Locate and identify every blood parasite.
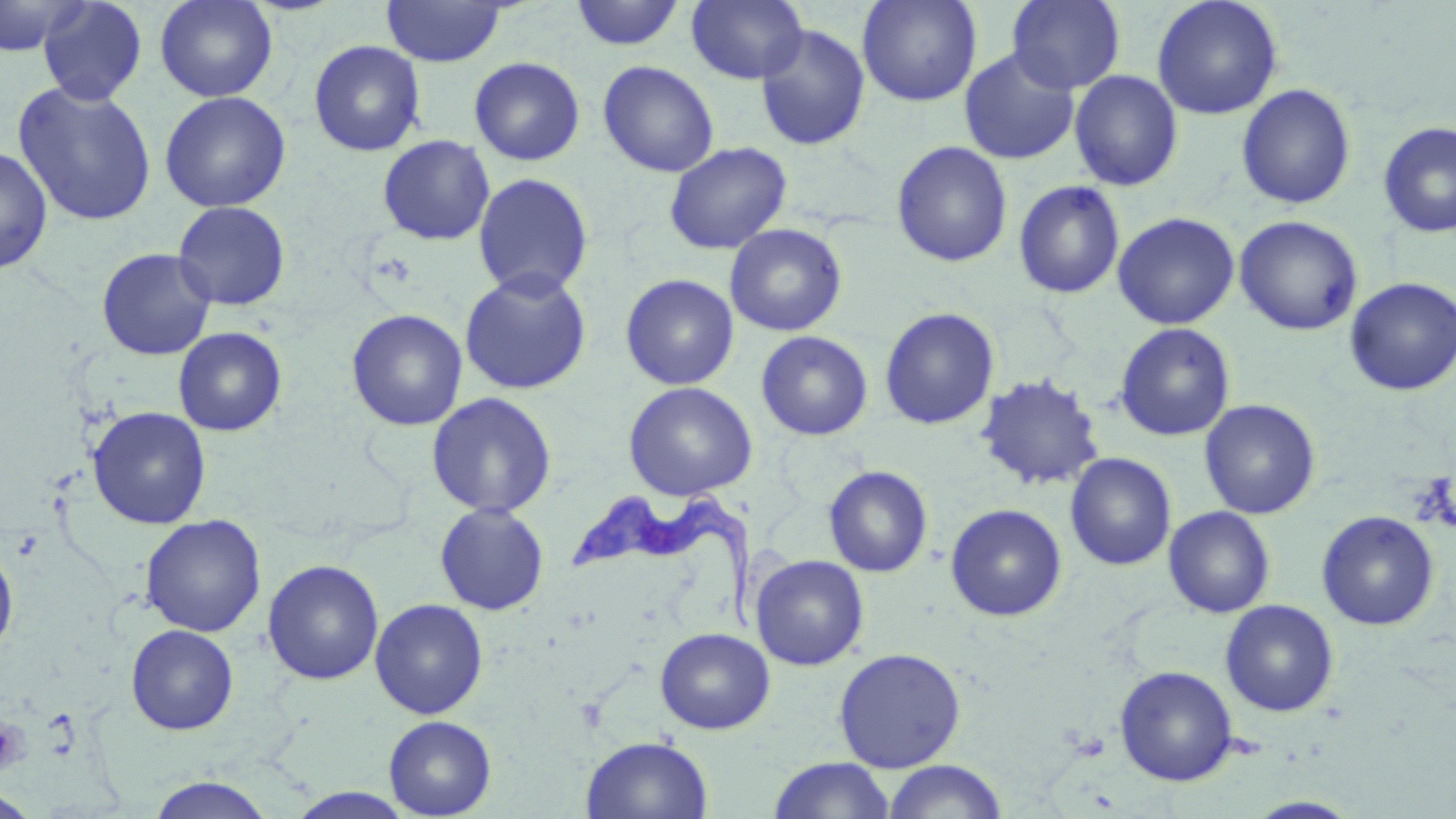
Approximate bounding boxes as named x1/y1/x2/y2 corners in pixels.
Trypanosoma brucei: (x1=568, y1=490, x2=762, y2=636).
No Plasmodium falciparum, Plasmodium ovale, Plasmodium malariae, Plasmodium vivax, or Babesia divergens observed.

slide_level_diagnosis: Trypanosoma brucei
stain: May-Grünwald-Giemsa
uninfected_red_blood_cell_locations: 'approximate bounding boxes as named x1/y1/x2/y2 corners in pixels: (x1=0, y1=0, x2=87, y2=57), (x1=37, y1=0, x2=148, y2=106), (x1=155, y1=0, x2=277, y2=102), (x1=381, y1=0, x2=508, y2=67), (x1=687, y1=0, x2=808, y2=84), (x1=856, y1=0, x2=983, y2=107), (x1=1006, y1=0, x2=1126, y2=94), (x1=1151, y1=0, x2=1284, y2=120), (x1=569, y1=1, x2=686, y2=51), (x1=755, y1=23, x2=871, y2=151), (x1=308, y1=40, x2=426, y2=157), (x1=959, y1=47, x2=1080, y2=165), (x1=468, y1=56, x2=585, y2=166), (x1=598, y1=60, x2=719, y2=177), (x1=1069, y1=70, x2=1183, y2=191), (x1=12, y1=81, x2=157, y2=226), (x1=1236, y1=84, x2=1356, y2=210), (x1=159, y1=91, x2=291, y2=213), (x1=1377, y1=122, x2=1456, y2=238), (x1=377, y1=134, x2=495, y2=246), (x1=664, y1=141, x2=792, y2=254), (x1=891, y1=141, x2=1013, y2=268), (x1=0, y1=146, x2=53, y2=274), (x1=472, y1=172, x2=594, y2=299), (x1=1013, y1=180, x2=1125, y2=299), (x1=172, y1=201, x2=291, y2=311), (x1=1113, y1=212, x2=1240, y2=330), (x1=1234, y1=215, x2=1363, y2=336), (x1=724, y1=223, x2=848, y2=336), (x1=96, y1=247, x2=217, y2=360), (x1=459, y1=268, x2=593, y2=395), (x1=620, y1=273, x2=739, y2=390), (x1=1344, y1=277, x2=1456, y2=396), (x1=879, y1=307, x2=1000, y2=430), (x1=346, y1=309, x2=468, y2=431), (x1=1114, y1=322, x2=1235, y2=442), (x1=173, y1=327, x2=287, y2=436), (x1=755, y1=331, x2=874, y2=441), (x1=976, y1=373, x2=1104, y2=491), (x1=622, y1=381, x2=758, y2=501), (x1=426, y1=392, x2=558, y2=518), (x1=1199, y1=398, x2=1321, y2=519), (x1=87, y1=407, x2=212, y2=530), (x1=1065, y1=452, x2=1177, y2=571), (x1=823, y1=465, x2=933, y2=578), (x1=433, y1=502, x2=550, y2=615), (x1=945, y1=503, x2=1068, y2=622), (x1=1163, y1=506, x2=1275, y2=618), (x1=1316, y1=511, x2=1439, y2=631), (x1=140, y1=514, x2=266, y2=637), (x1=0, y1=541, x2=18, y2=665), (x1=751, y1=554, x2=870, y2=671), (x1=263, y1=559, x2=384, y2=685), (x1=370, y1=598, x2=489, y2=719), (x1=1220, y1=600, x2=1339, y2=717), (x1=125, y1=624, x2=239, y2=735), (x1=655, y1=627, x2=775, y2=734), (x1=833, y1=647, x2=966, y2=772), (x1=1114, y1=665, x2=1239, y2=786), (x1=383, y1=715, x2=496, y2=818), (x1=581, y1=735, x2=713, y2=818), (x1=768, y1=757, x2=895, y2=818), (x1=881, y1=759, x2=1008, y2=819), (x1=146, y1=775, x2=276, y2=818), (x1=0, y1=788, x2=44, y2=818), (x1=287, y1=788, x2=416, y2=818), (x1=1245, y1=796, x2=1362, y2=818)'
magnification: 1000x
preparation: thin blood smear
modality: optical microscopy
image_size: 1456×819 pixels
platelet_locations: 'approximate bounding boxes as named x1/y1/x2/y2 corners in pixels: (x1=0, y1=718, x2=30, y2=777)'
field_of_view: one of a larger specimen